Report the malaria status of this cell.
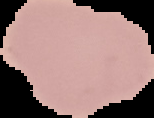
It is uninfected.

image_type: segmented cell region on a black background
preparation: thin blood smear
image_size: 154×118 pixels